Locate every uninfected red blood cell.
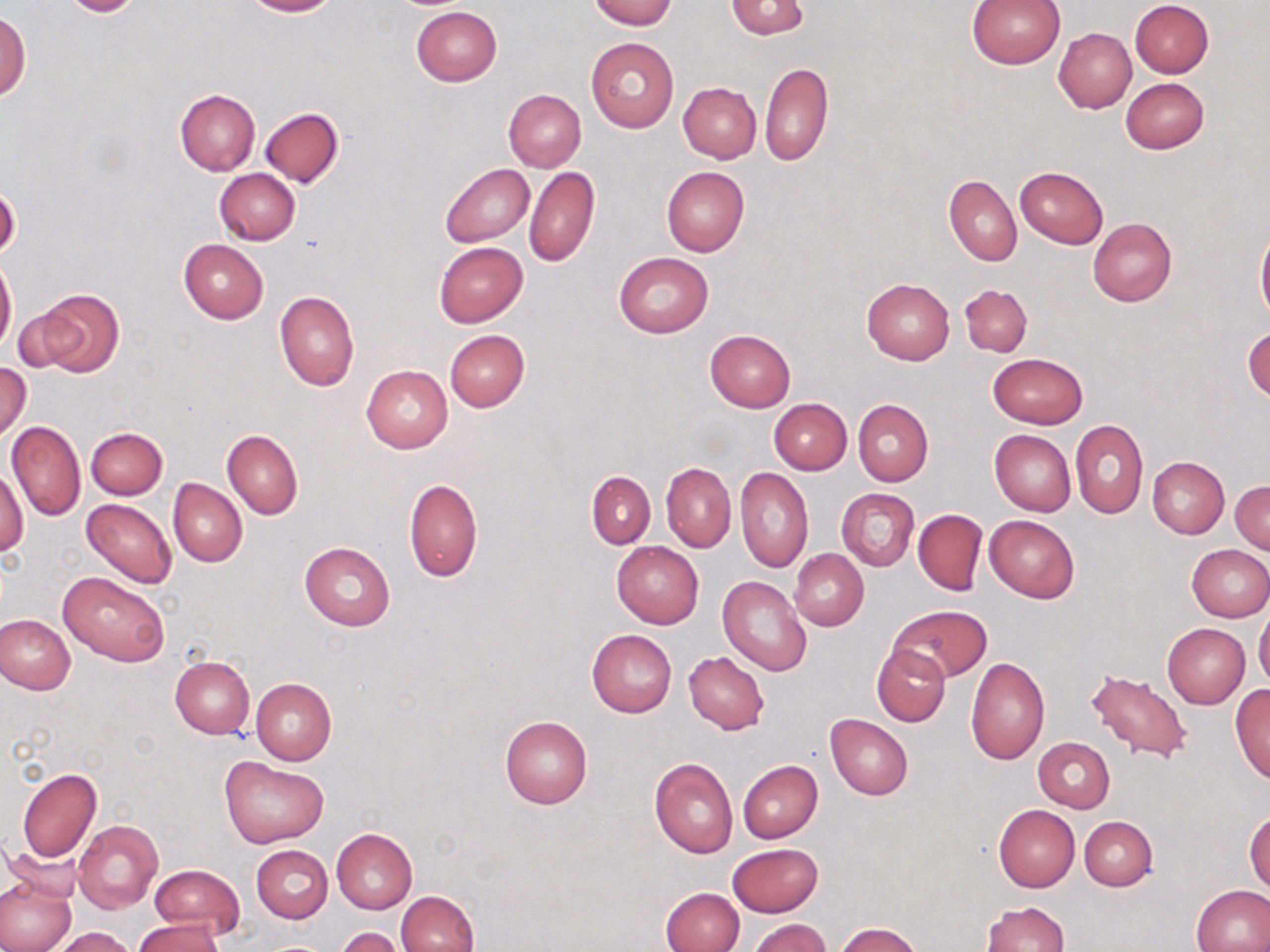

Approximate bounding boxes as [x1, y1, x2, y2] in pixels.
Uninfected red blood cells: [60, 0, 145, 17], [243, 0, 338, 16], [590, 0, 677, 29], [966, 0, 1064, 68], [1131, 0, 1213, 78], [724, 1, 810, 39], [411, 5, 502, 86], [0, 10, 31, 101], [1054, 27, 1136, 113], [586, 37, 679, 132], [760, 62, 833, 166], [1120, 78, 1208, 154], [678, 82, 761, 163], [175, 89, 260, 175], [503, 89, 585, 172], [259, 109, 342, 187], [440, 162, 535, 246], [524, 166, 600, 267], [661, 166, 749, 256], [1015, 166, 1108, 248], [214, 168, 301, 245], [943, 175, 1021, 265], [1087, 217, 1176, 307], [1256, 223, 1270, 322], [179, 239, 268, 323], [434, 242, 527, 326], [613, 251, 714, 338], [0, 257, 17, 352], [861, 278, 954, 365], [960, 284, 1032, 356], [30, 289, 125, 377], [275, 291, 359, 391], [1244, 324, 1270, 404], [445, 329, 530, 411], [704, 329, 795, 412], [988, 353, 1087, 428], [0, 363, 31, 443], [361, 365, 453, 452], [769, 399, 852, 475], [853, 399, 933, 485], [1070, 419, 1147, 519], [6, 420, 86, 521], [85, 428, 167, 499], [990, 429, 1077, 516], [223, 430, 303, 519], [1147, 457, 1228, 538], [662, 463, 735, 551], [1, 468, 28, 559], [734, 469, 813, 573], [586, 471, 655, 547], [168, 478, 247, 567], [404, 478, 482, 583], [1231, 479, 1270, 554], [838, 487, 918, 571], [82, 498, 177, 589], [913, 509, 986, 595], [984, 515, 1080, 604], [300, 541, 395, 630], [611, 541, 703, 629], [1186, 544, 1270, 621], [790, 549, 868, 630], [59, 573, 169, 667], [719, 576, 812, 676], [889, 605, 992, 684], [1254, 608, 1270, 691], [1, 615, 75, 694], [1161, 623, 1250, 706], [587, 629, 676, 717], [872, 644, 950, 727], [684, 652, 769, 735], [169, 656, 255, 739], [965, 656, 1049, 764], [1087, 668, 1194, 765], [250, 677, 336, 764], [1231, 686, 1270, 784], [825, 715, 912, 800], [499, 716, 592, 810], [1034, 737, 1115, 811], [220, 756, 329, 848], [650, 757, 738, 858], [738, 760, 824, 843], [17, 767, 101, 862], [994, 805, 1079, 891], [1246, 809, 1270, 892], [1079, 816, 1158, 891], [73, 819, 163, 914], [332, 828, 417, 914], [727, 843, 823, 917], [250, 844, 333, 922], [150, 865, 245, 939], [0, 877, 75, 952], [1191, 884, 1270, 952], [660, 887, 743, 952], [394, 891, 478, 952], [981, 902, 1068, 952], [750, 918, 831, 952], [133, 919, 224, 952], [835, 923, 922, 952], [51, 927, 140, 952], [335, 927, 407, 952].

Summary:
  - Slide-level diagnosis: negative for blood parasites
  - Field of view: one of a larger specimen
  - Preparation: thin blood smear
  - Image size: 1270×952 pixels
  - Magnification: 1000x
  - Modality: light microscopy
  - Stain: May-Grünwald-Giemsa